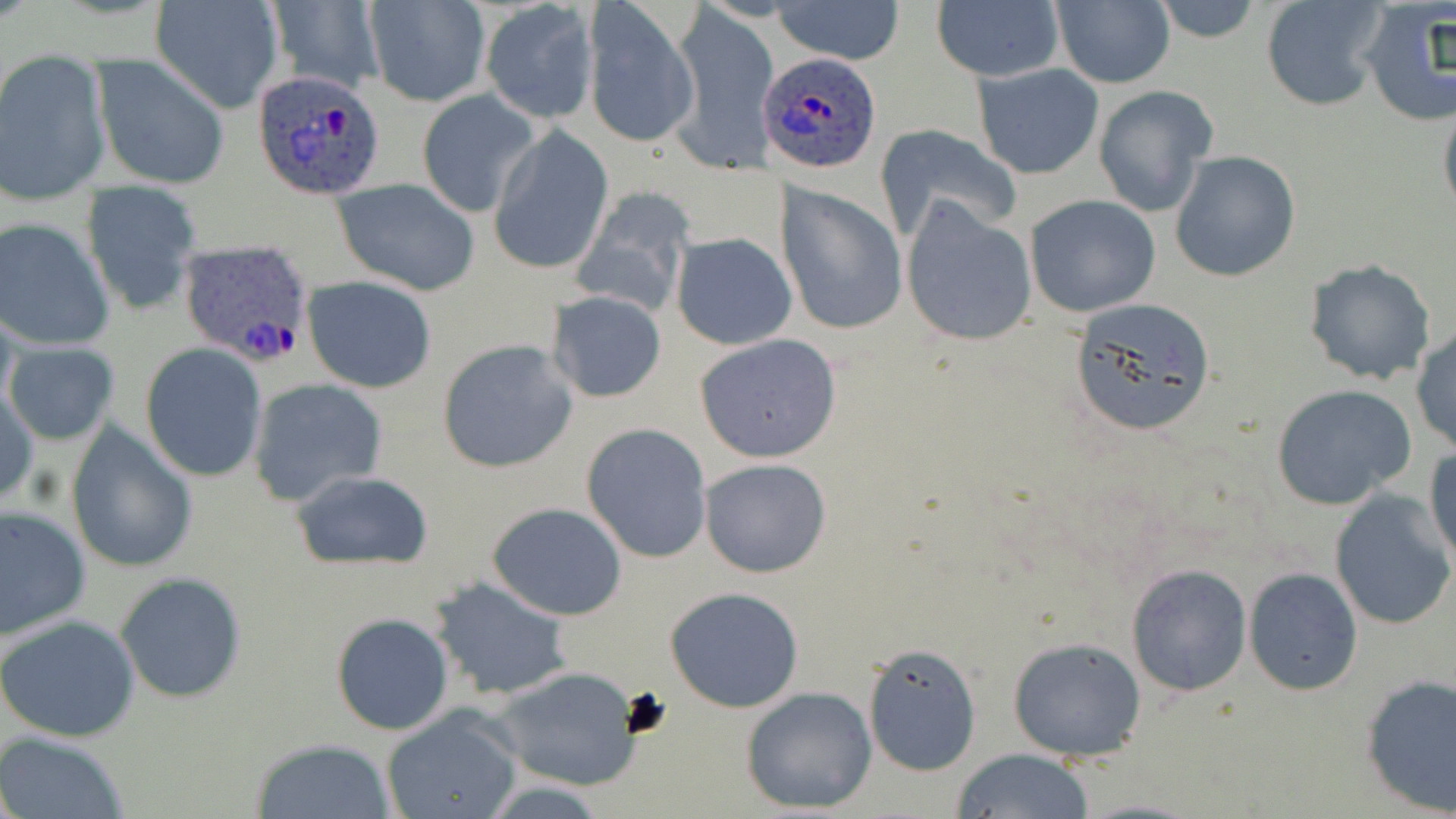

Summary:
  - Coordinate format: approximate bounding boxes as (x1, y1, x2, y2) in pixels
  - Platelet locations: (621, 687, 675, 738)
  - Uninfected red blood cell locations: (150, 0, 285, 114), (363, 0, 491, 107), (770, 0, 905, 66), (1151, 0, 1264, 44), (1262, 0, 1389, 111), (1049, 1, 1175, 88), (263, 2, 384, 91), (479, 2, 598, 125), (931, 2, 1064, 82), (1356, 2, 1455, 126), (665, 3, 781, 175), (583, 4, 699, 150), (0, 52, 109, 201), (95, 58, 230, 190), (973, 63, 1104, 178), (1094, 86, 1215, 217), (415, 89, 539, 219), (1439, 98, 1456, 223), (876, 123, 1022, 243), (487, 126, 614, 276), (1170, 150, 1300, 283), (332, 179, 483, 295), (81, 183, 202, 317), (777, 184, 908, 336), (570, 190, 696, 319), (1024, 194, 1163, 319), (900, 197, 1036, 347), (0, 217, 113, 351), (672, 233, 796, 349), (1303, 259, 1437, 385), (302, 274, 437, 393), (546, 291, 667, 404), (1068, 298, 1220, 437), (1411, 326, 1456, 455), (693, 332, 842, 462), (438, 339, 577, 473), (6, 344, 118, 445), (141, 344, 267, 482), (248, 379, 389, 507), (1271, 382, 1418, 509), (1, 384, 39, 508), (581, 423, 713, 563), (66, 425, 198, 575), (1425, 445, 1456, 574), (699, 457, 831, 578), (288, 469, 435, 571), (1329, 491, 1454, 632), (487, 502, 629, 621), (1, 506, 91, 641), (1125, 562, 1253, 698), (1243, 566, 1363, 697), (115, 572, 247, 704), (429, 576, 572, 701), (663, 587, 805, 713), (331, 613, 453, 735), (1, 614, 140, 742), (1007, 636, 1147, 762), (862, 642, 981, 777), (490, 666, 644, 791), (1359, 673, 1456, 815), (741, 686, 878, 814), (381, 706, 525, 819), (2, 733, 129, 819), (249, 737, 397, 819), (951, 747, 1096, 819)
  - Plasmodium ovale-infected red blood cell locations: (759, 52, 883, 173), (251, 70, 388, 202), (177, 240, 317, 366)
  - Slide-level diagnosis: Plasmodium ovale
  - Magnification: 1000x
  - Image size: 1456×819 pixels
  - Field of view: single
  - Preparation: thin blood smear
  - Stain: May-Grünwald-Giemsa
  - Modality: light microscopy